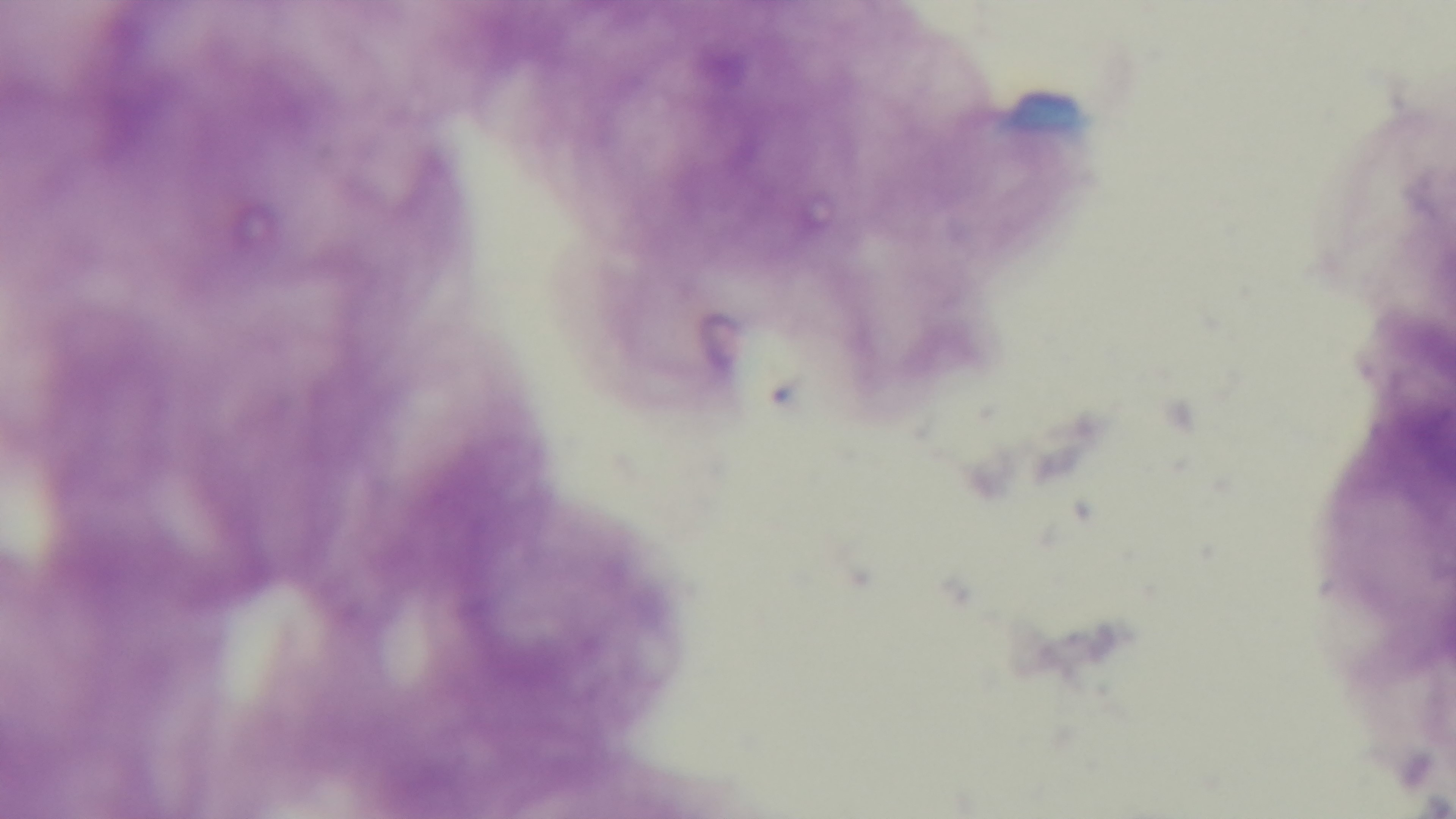 Light microscopy. Preparation: thick. Single field of view. Captured with a mounted 4K digital camera. Malaria status: negative. Giemsa-stained. Oil-immersion objective, 100x.